Name the blood parasite species.
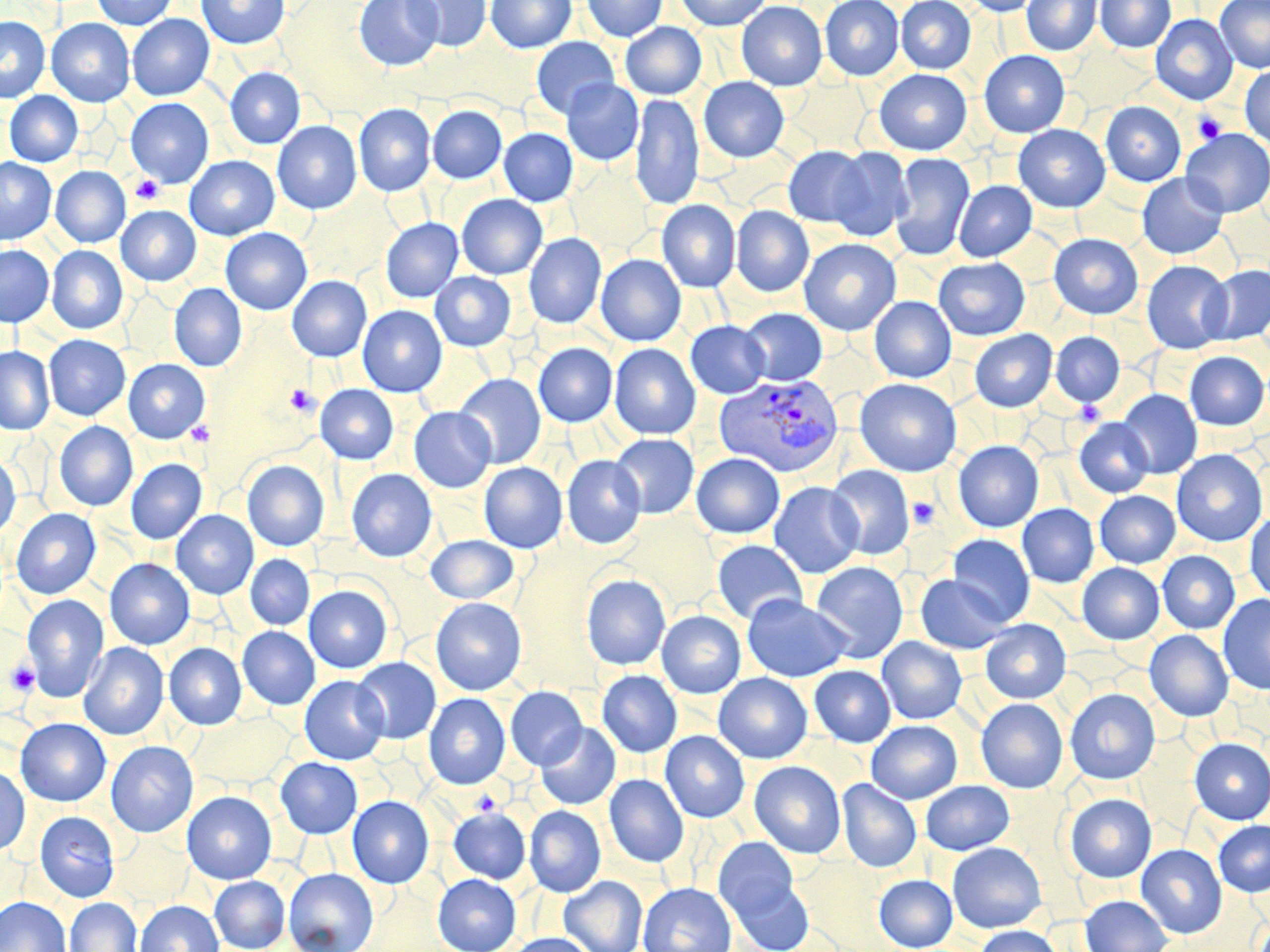
Plasmodium vivax.

Summary:
  - Coordinate format: approximate bounding boxes as [x1, y1, x2, y2] in pixels
  - Plasmodium vivax-infected red blood cell locations: [712, 373, 844, 477]
  - Uninfected red blood cell locations: [92, 0, 178, 30], [196, 0, 290, 49], [354, 0, 444, 71], [404, 0, 492, 51], [486, 0, 576, 53], [581, 0, 668, 42], [675, 0, 771, 30], [820, 0, 904, 80], [896, 0, 975, 74], [960, 0, 1044, 17], [1022, 0, 1102, 56], [1095, 0, 1176, 52], [737, 1, 827, 90], [1216, 1, 1270, 72], [127, 14, 214, 100], [1151, 14, 1238, 105], [0, 16, 50, 103], [46, 18, 135, 106], [620, 22, 707, 100], [531, 36, 619, 119], [979, 50, 1069, 138], [1240, 65, 1270, 148], [225, 67, 304, 148], [874, 69, 971, 155], [699, 77, 789, 162], [789, 78, 870, 150], [561, 79, 644, 166], [4, 91, 83, 166], [631, 93, 704, 209], [125, 98, 214, 188], [1101, 102, 1186, 186], [354, 103, 435, 196], [428, 106, 506, 183], [272, 121, 362, 214], [1013, 124, 1110, 212], [499, 128, 578, 206], [1181, 128, 1270, 217], [783, 145, 871, 227], [829, 147, 913, 241], [890, 152, 975, 260], [185, 156, 279, 240], [0, 158, 56, 244], [50, 166, 131, 248], [569, 167, 657, 251], [1137, 173, 1228, 259], [954, 180, 1037, 261], [298, 194, 397, 284], [457, 194, 547, 279], [657, 200, 740, 292], [116, 205, 201, 286], [731, 206, 814, 296], [381, 218, 463, 302], [220, 228, 312, 314], [1049, 233, 1142, 319], [524, 234, 606, 328], [799, 238, 901, 335], [0, 245, 54, 327], [47, 245, 128, 334], [596, 254, 686, 346], [934, 257, 1029, 340], [1142, 260, 1233, 354], [1203, 265, 1270, 345], [430, 271, 516, 351], [287, 276, 372, 362], [169, 284, 247, 371], [869, 296, 956, 383], [358, 305, 447, 397], [741, 308, 827, 385], [685, 320, 770, 399], [970, 329, 1057, 411], [1051, 332, 1125, 406], [44, 335, 130, 421], [534, 343, 617, 427], [609, 343, 701, 440], [0, 346, 55, 435], [1184, 351, 1269, 430], [123, 359, 210, 443], [455, 374, 546, 468], [855, 378, 961, 476], [315, 384, 398, 464], [1118, 389, 1202, 478], [409, 407, 496, 492], [1074, 418, 1154, 498], [54, 421, 137, 511], [610, 433, 699, 518], [953, 440, 1044, 532], [1171, 449, 1268, 546], [0, 453, 21, 540], [691, 453, 784, 539], [562, 455, 646, 549], [126, 459, 207, 544], [242, 460, 329, 551], [479, 462, 568, 552], [826, 465, 915, 560], [346, 469, 437, 562], [769, 482, 864, 578], [1094, 490, 1180, 567], [1017, 504, 1099, 587], [11, 508, 100, 599], [171, 510, 258, 599], [1245, 510, 1270, 602], [948, 534, 1035, 625], [426, 535, 519, 604], [712, 540, 808, 624], [1158, 551, 1240, 634], [245, 554, 314, 630], [105, 559, 194, 649], [811, 561, 908, 663], [1077, 563, 1164, 644], [581, 574, 670, 669], [915, 574, 1011, 654], [304, 585, 392, 673], [21, 594, 109, 703], [742, 594, 851, 682], [1218, 594, 1270, 695], [431, 597, 527, 695], [657, 610, 746, 698], [980, 619, 1071, 703], [238, 626, 320, 709], [1145, 630, 1233, 721], [877, 637, 967, 724], [78, 642, 169, 740], [164, 643, 247, 730], [353, 657, 441, 744], [809, 665, 896, 747], [597, 670, 682, 757], [713, 673, 812, 763], [300, 675, 389, 764], [505, 686, 588, 770], [1065, 688, 1160, 784], [424, 693, 510, 789], [976, 698, 1068, 793], [190, 710, 294, 788], [14, 718, 111, 807], [866, 720, 962, 803], [536, 722, 621, 810], [660, 731, 749, 822], [1189, 738, 1270, 825], [106, 741, 198, 837], [276, 757, 362, 838], [750, 761, 846, 858], [0, 764, 30, 856], [604, 774, 689, 867], [837, 778, 922, 872], [921, 780, 1014, 854], [182, 791, 277, 884], [1065, 793, 1157, 882], [347, 796, 434, 888], [524, 806, 606, 897], [448, 807, 530, 884], [34, 811, 120, 902], [1214, 820, 1270, 897], [114, 831, 192, 907], [714, 838, 800, 923], [947, 842, 1046, 932], [1136, 844, 1226, 938], [284, 868, 378, 952], [433, 873, 521, 952], [874, 874, 957, 951], [210, 876, 289, 951], [558, 876, 648, 952], [730, 877, 814, 952], [638, 882, 736, 952], [1080, 894, 1172, 952], [0, 896, 71, 952], [65, 897, 141, 952], [135, 900, 223, 952], [974, 925, 1063, 952], [504, 933, 596, 952]
  - Platelet locations: [1193, 112, 1226, 144], [130, 175, 163, 204], [284, 384, 320, 416], [1072, 400, 1106, 425], [186, 421, 214, 446], [907, 496, 940, 529], [4, 656, 40, 699], [470, 791, 501, 817]
  - Modality: optical microscopy
  - Stain: May-Grünwald-Giemsa
  - Field of view: one of a larger specimen
  - Magnification: 1000x
  - Image size: 1270×952 pixels
  - Preparation: thin blood smear